State the blood parasite species.
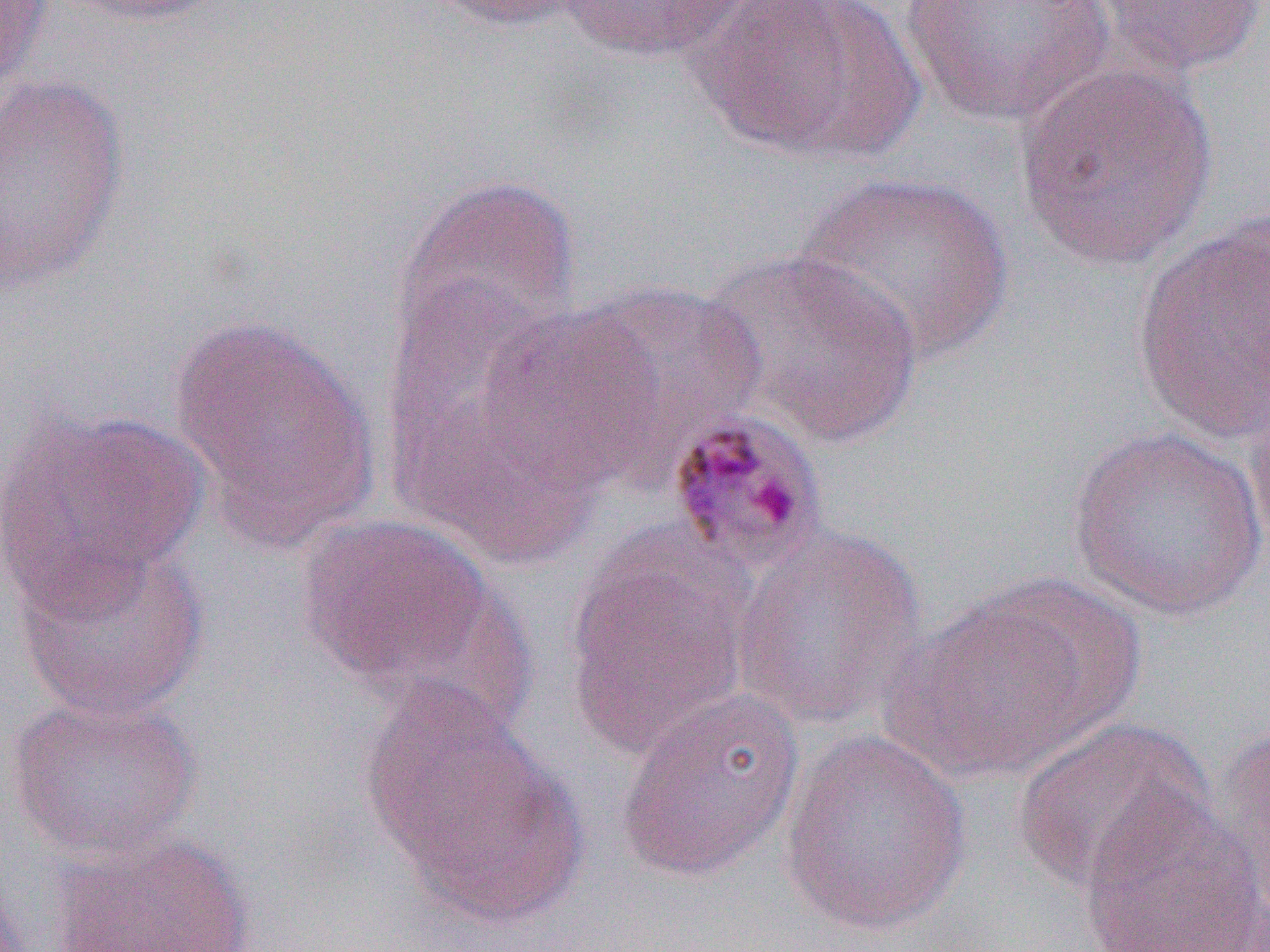
Plasmodium malariae.

Summary:
  - Coordinate format: approximate bounding boxes as named x1/y1/x2/y2 corners in pixels
  - Uninfected red blood cell locations: (x1=0, y1=0, x2=53, y2=96), (x1=59, y1=0, x2=230, y2=27), (x1=422, y1=0, x2=598, y2=31), (x1=552, y1=0, x2=754, y2=65), (x1=694, y1=0, x2=922, y2=163), (x1=898, y1=0, x2=1119, y2=128), (x1=1093, y1=0, x2=1265, y2=76), (x1=1013, y1=63, x2=1221, y2=270), (x1=0, y1=73, x2=130, y2=295), (x1=795, y1=171, x2=1012, y2=366), (x1=390, y1=174, x2=581, y2=365), (x1=1130, y1=215, x2=1270, y2=449), (x1=700, y1=247, x2=924, y2=448), (x1=569, y1=280, x2=767, y2=467), (x1=476, y1=303, x2=664, y2=491), (x1=171, y1=313, x2=380, y2=547), (x1=1244, y1=377, x2=1270, y2=568), (x1=392, y1=386, x2=603, y2=569), (x1=2, y1=405, x2=208, y2=616), (x1=1067, y1=425, x2=1269, y2=619), (x1=295, y1=513, x2=502, y2=696), (x1=733, y1=525, x2=930, y2=730), (x1=11, y1=536, x2=211, y2=722), (x1=565, y1=540, x2=756, y2=760), (x1=972, y1=575, x2=1146, y2=741), (x1=886, y1=589, x2=1108, y2=783), (x1=363, y1=680, x2=577, y2=919), (x1=614, y1=688, x2=805, y2=884), (x1=5, y1=692, x2=202, y2=862), (x1=1010, y1=717, x2=1215, y2=896), (x1=1212, y1=720, x2=1270, y2=932), (x1=778, y1=729, x2=973, y2=937), (x1=1076, y1=788, x2=1268, y2=952), (x1=46, y1=832, x2=257, y2=952)
  - Plasmodium malariae-infected red blood cell locations: (x1=663, y1=407, x2=832, y2=578)
  - Preparation: thin blood smear
  - Modality: optical microscopy
  - Image size: 1270×952 pixels
  - Field of view: one of a larger specimen
  - Magnification: 1000x